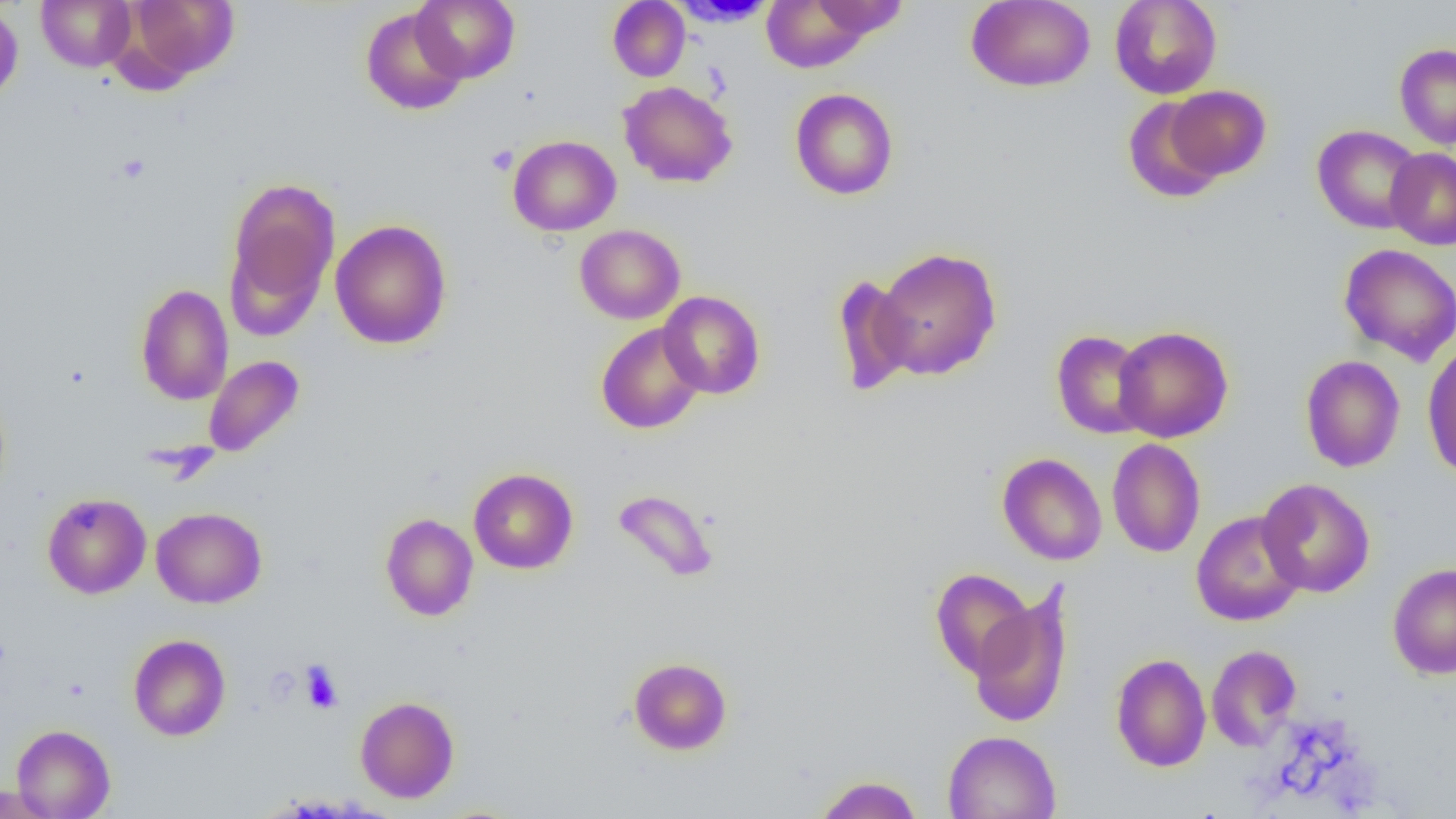

Approximate bounding boxes as (x1,y1)-(x2,y2) corner pairs in pixels. Platelet locations: (486,145)-(518,175), (300,661)-(343,713). Uninfected red blood cell locations: (36,0)-(136,72), (120,0)-(239,85), (412,0)-(520,83), (607,0)-(690,82), (760,0)-(875,73), (966,0)-(1095,92), (1109,0)-(1222,99), (669,1)-(778,27), (811,1)-(908,40), (0,3)-(23,105), (360,7)-(469,115), (1394,44)-(1456,149), (618,81)-(737,188), (1166,85)-(1271,182), (789,88)-(899,200), (1122,96)-(1225,203), (1312,125)-(1424,234), (507,135)-(621,236), (1385,147)-(1456,250), (225,177)-(340,320), (330,219)-(452,349), (574,224)-(685,324), (1338,243)-(1456,366), (872,247)-(1002,381), (831,274)-(917,397), (135,284)-(233,405), (658,291)-(766,399), (596,323)-(706,434), (1113,325)-(1234,442), (1051,330)-(1153,439), (1422,340)-(1456,480), (203,355)-(304,457), (1300,355)-(1405,473), (1107,438)-(1205,558), (997,452)-(1107,565), (468,468)-(578,574), (1256,478)-(1375,597), (612,488)-(719,583), (42,492)-(151,598), (151,507)-(266,608), (1191,510)-(1306,627), (380,513)-(478,621), (1387,563)-(1456,679), (930,567)-(1035,679), (969,587)-(1075,728), (128,634)-(231,741), (1206,644)-(1301,751), (1111,653)-(1211,772), (629,657)-(732,755), (355,696)-(459,802), (12,724)-(115,818), (942,730)-(1062,818), (814,775)-(923,819), (0,783)-(60,816). Slide-level diagnosis: no evidence of blood parasites. Image is 1456×819 pixels. Single field of view. Thin blood smear. Light microscopy. Captured at 1000x magnification.